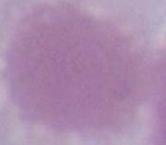
Summary:
  - Modality: micrograph
  - Identification: red blood cell
  - Magnification: 1000x